Locate every WBC.
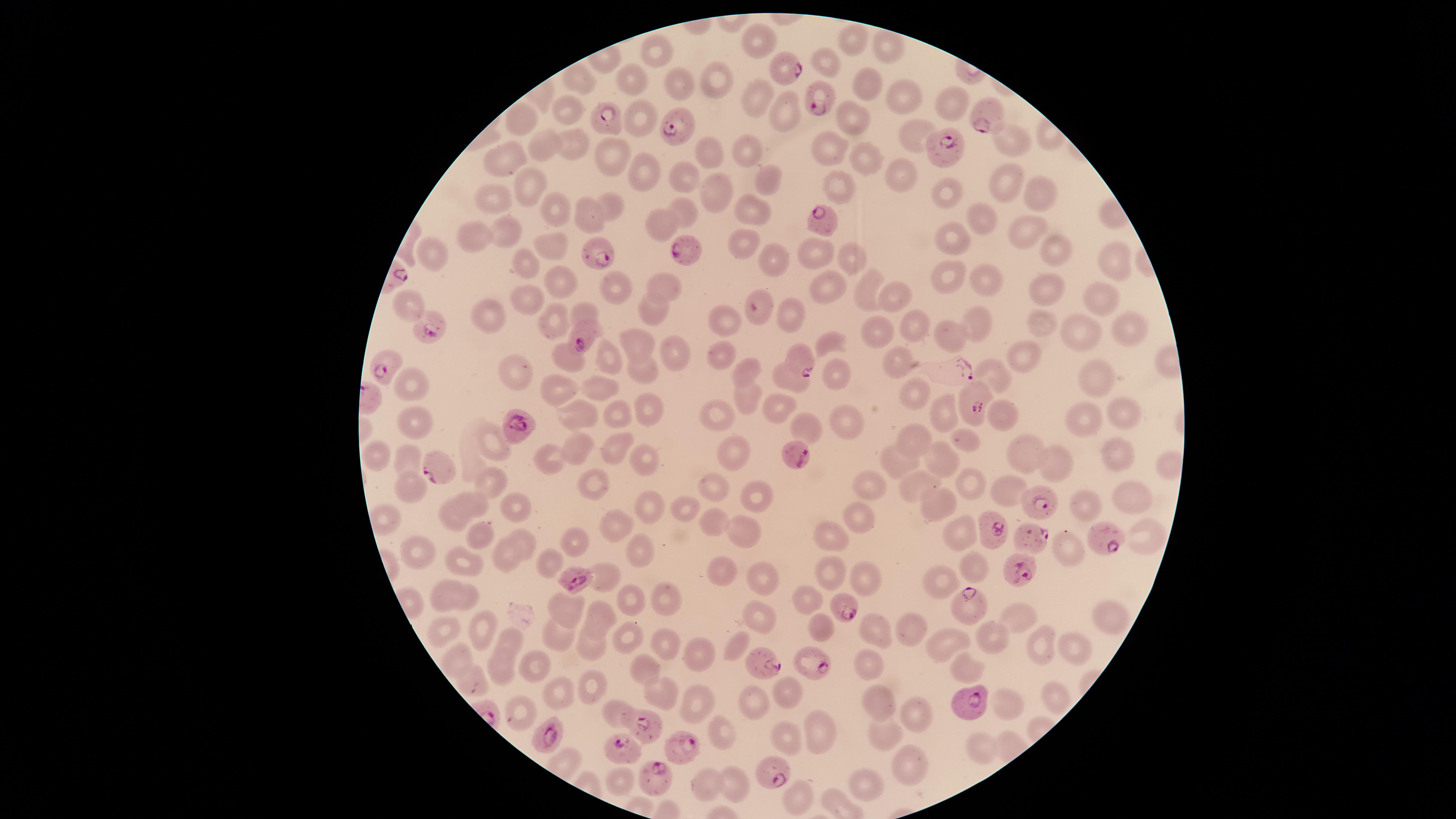
No WBCs identified.

Approximate marker points, in pixels from the top-left corner.
Summary:
  - Parasitized RBCs: (x=779, y=70), (x=816, y=98), (x=984, y=116), (x=603, y=118), (x=674, y=125), (x=946, y=152), (x=818, y=215), (x=689, y=253), (x=596, y=256), (x=430, y=324), (x=578, y=336), (x=799, y=357), (x=387, y=364), (x=959, y=367), (x=970, y=404), (x=517, y=423), (x=795, y=455), (x=433, y=468), (x=1042, y=501), (x=988, y=526), (x=1027, y=535), (x=1100, y=535), (x=1022, y=564), (x=578, y=576), (x=843, y=604), (x=976, y=606), (x=814, y=661), (x=763, y=664), (x=970, y=701), (x=641, y=724), (x=550, y=731), (x=684, y=747), (x=623, y=750), (x=769, y=772), (x=653, y=775)
  - Uninfected RBCs: (x=757, y=37), (x=851, y=42), (x=660, y=50), (x=887, y=50), (x=827, y=57), (x=632, y=79), (x=578, y=80), (x=713, y=80), (x=677, y=87), (x=858, y=88), (x=752, y=96), (x=908, y=97), (x=948, y=104), (x=785, y=110), (x=569, y=111), (x=521, y=117), (x=848, y=118), (x=640, y=122), (x=912, y=133), (x=547, y=143), (x=1015, y=144), (x=567, y=146), (x=831, y=148), (x=707, y=154), (x=746, y=154), (x=612, y=156), (x=864, y=157), (x=497, y=160), (x=644, y=175), (x=770, y=176), (x=684, y=178), (x=897, y=179), (x=835, y=180), (x=526, y=185), (x=1003, y=186), (x=714, y=190), (x=946, y=193), (x=493, y=197), (x=1044, y=197), (x=609, y=204), (x=554, y=207), (x=682, y=211), (x=754, y=211), (x=584, y=218), (x=988, y=224), (x=663, y=226), (x=1014, y=227), (x=503, y=230), (x=947, y=233), (x=473, y=236), (x=736, y=241), (x=554, y=247), (x=815, y=250), (x=430, y=251), (x=1057, y=252), (x=849, y=256), (x=1113, y=256), (x=771, y=260), (x=525, y=264), (x=947, y=275), (x=988, y=278), (x=564, y=285), (x=664, y=286), (x=828, y=286), (x=866, y=287), (x=1041, y=293), (x=1102, y=293), (x=892, y=296), (x=758, y=298), (x=414, y=303), (x=523, y=304), (x=580, y=311), (x=649, y=312), (x=793, y=316), (x=489, y=319), (x=551, y=320), (x=728, y=320), (x=980, y=325), (x=909, y=327), (x=1040, y=327), (x=1118, y=328), (x=1075, y=331), (x=877, y=334), (x=952, y=337), (x=833, y=342), (x=638, y=345), (x=718, y=352), (x=670, y=353), (x=1020, y=353), (x=608, y=356), (x=896, y=362), (x=568, y=364), (x=641, y=370), (x=746, y=371), (x=990, y=371), (x=830, y=373), (x=518, y=375), (x=1091, y=376), (x=784, y=379), (x=412, y=382), (x=599, y=388), (x=555, y=391), (x=915, y=393), (x=742, y=399), (x=778, y=407), (x=638, y=409), (x=573, y=412), (x=938, y=412), (x=612, y=414), (x=1128, y=414), (x=721, y=416), (x=1009, y=416), (x=1087, y=417), (x=845, y=421), (x=418, y=424), (x=799, y=428), (x=919, y=439), (x=493, y=441), (x=967, y=442), (x=572, y=447), (x=729, y=448), (x=614, y=450), (x=1118, y=453), (x=374, y=455), (x=1028, y=455), (x=408, y=456), (x=643, y=456), (x=943, y=457), (x=545, y=458), (x=897, y=464), (x=1056, y=470), (x=595, y=478), (x=489, y=485), (x=916, y=485), (x=968, y=485), (x=409, y=486), (x=718, y=488), (x=875, y=490), (x=1005, y=492), (x=755, y=493), (x=1126, y=499), (x=471, y=502), (x=1085, y=505), (x=682, y=506), (x=933, y=506), (x=516, y=507), (x=650, y=507), (x=448, y=515), (x=711, y=517), (x=856, y=521), (x=741, y=529), (x=612, y=532), (x=1145, y=533), (x=958, y=535), (x=481, y=536), (x=831, y=539), (x=524, y=542), (x=572, y=545), (x=639, y=549), (x=421, y=551), (x=502, y=554), (x=1065, y=558), (x=463, y=560), (x=549, y=565), (x=970, y=568), (x=831, y=569), (x=719, y=570), (x=764, y=577), (x=604, y=580), (x=864, y=581), (x=944, y=585), (x=444, y=593), (x=468, y=599), (x=668, y=599), (x=805, y=600), (x=632, y=604), (x=569, y=612), (x=601, y=613), (x=755, y=618), (x=1017, y=618), (x=1107, y=619), (x=478, y=625), (x=444, y=626), (x=906, y=627), (x=822, y=628), (x=875, y=632), (x=557, y=634), (x=628, y=636), (x=994, y=637), (x=664, y=638), (x=507, y=641), (x=737, y=645), (x=943, y=645), (x=590, y=648), (x=1071, y=648), (x=1041, y=651), (x=453, y=654), (x=692, y=656), (x=538, y=666), (x=500, y=667), (x=640, y=669), (x=869, y=669), (x=966, y=669), (x=472, y=677), (x=594, y=686), (x=786, y=690), (x=558, y=693), (x=665, y=694), (x=1044, y=696), (x=699, y=704), (x=878, y=705), (x=753, y=706), (x=1008, y=707), (x=521, y=712), (x=616, y=713), (x=912, y=715), (x=723, y=729), (x=815, y=735), (x=881, y=738), (x=786, y=739), (x=980, y=751), (x=904, y=762), (x=622, y=783), (x=736, y=784), (x=861, y=785), (x=715, y=789), (x=796, y=798)
  - Image size: 1456×819 pixels
  - Visible region: circular
  - Field of view: single
  - Stain: Giemsa
  - Species: Plasmodium falciparum
  - Presence: malaria parasites detected
  - Preparation: thin blood film
  - Capture: smartphone photograph through the microscope eyepiece